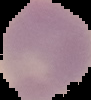 Cell region segmented out of the field of view; the surrounding area is masked to black. Malaria status: uninfected. From a thin blood film. Image is 91×100 pixels.